Classify this cell by malaria status.
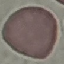

Uninfected.

capture = smartphone camera at the microscope eyepiece
stain = Giemsa
preparation = thin blood smear
image type = automatically extracted cell patch, resized to 64 × 64 pixels